Locate every white blood cell.
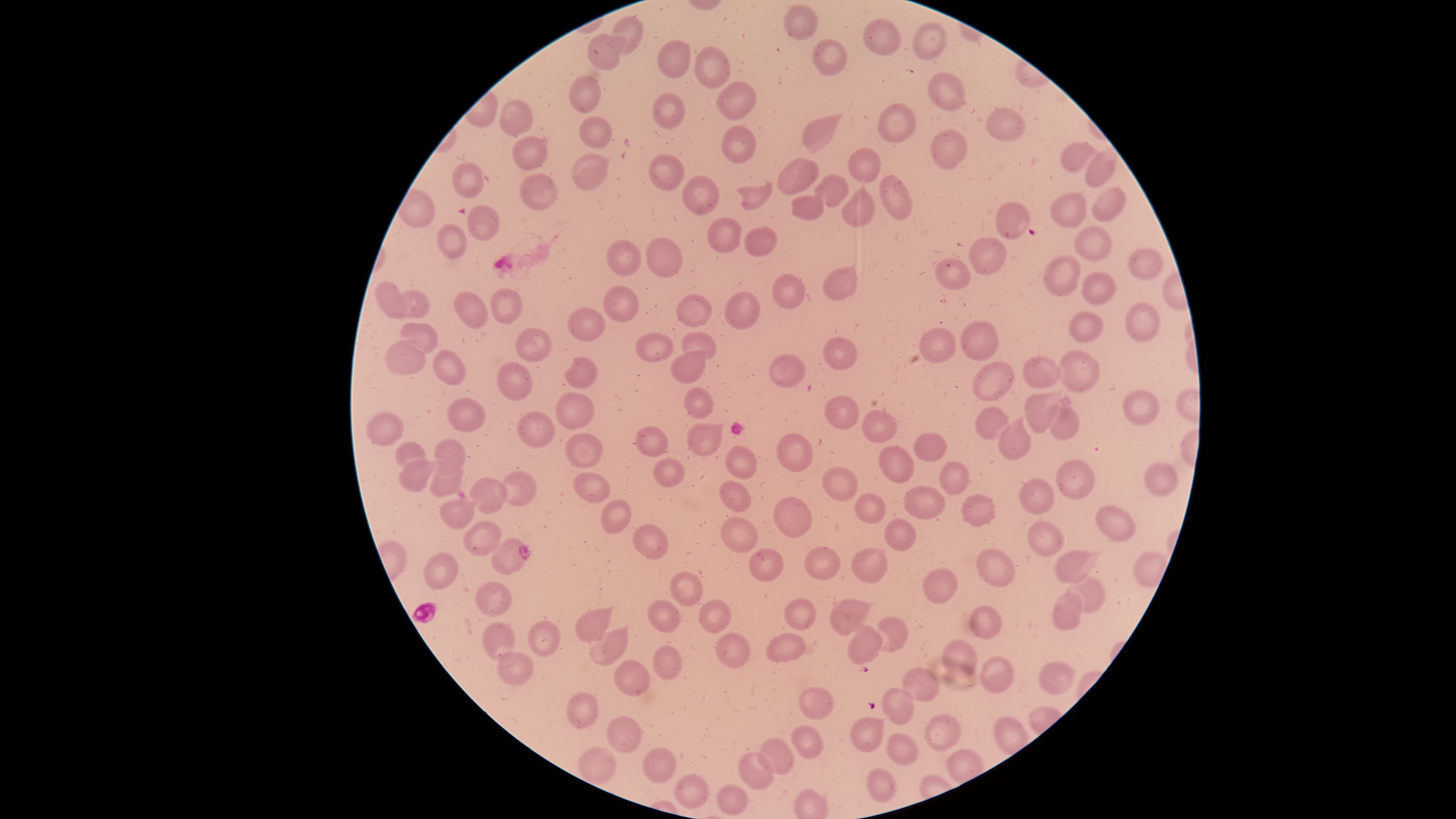
No white blood cells identified.

{
  "stain": "Giemsa",
  "field_of_view": "single",
  "presence": "no malaria parasites identified",
  "uninfected_red_blood_cells": "approximate bounding boxes as [left, top, right, bottom] in pixels: [782, 3, 820, 41], [612, 16, 645, 57], [864, 19, 901, 55], [912, 23, 946, 60], [585, 33, 622, 72], [658, 39, 691, 78], [813, 39, 846, 76], [695, 47, 731, 89], [927, 72, 965, 111], [568, 75, 600, 114], [717, 81, 756, 120], [652, 93, 686, 131], [499, 99, 532, 135], [877, 104, 916, 143], [986, 109, 1026, 143], [802, 115, 840, 153], [579, 116, 611, 148], [721, 126, 755, 164], [931, 129, 966, 169], [512, 136, 547, 170], [1060, 140, 1101, 172], [848, 148, 880, 183], [1084, 151, 1116, 188], [572, 153, 609, 192], [649, 154, 683, 191], [778, 158, 820, 196], [451, 161, 485, 198], [519, 174, 555, 209], [815, 174, 849, 208], [879, 174, 912, 221], [681, 176, 717, 214], [736, 182, 773, 209], [1092, 187, 1124, 222], [841, 188, 875, 226], [1050, 192, 1086, 228], [789, 193, 824, 220], [995, 202, 1030, 240], [466, 205, 499, 240], [706, 217, 742, 254], [436, 223, 467, 258], [1074, 223, 1112, 262], [743, 228, 777, 256], [969, 235, 1005, 274], [645, 237, 682, 278], [605, 240, 641, 276], [1129, 248, 1162, 280], [1044, 256, 1081, 297], [934, 258, 972, 290], [823, 266, 856, 302], [772, 273, 806, 308], [1082, 274, 1116, 306], [374, 281, 409, 318], [602, 286, 637, 321], [490, 288, 521, 325], [394, 290, 429, 319], [725, 291, 761, 329], [454, 293, 489, 329], [676, 295, 710, 325], [1126, 305, 1159, 343], [569, 308, 605, 341], [1069, 311, 1104, 341], [962, 321, 998, 360], [400, 322, 436, 353], [515, 328, 552, 362], [919, 328, 955, 362], [682, 332, 716, 360], [636, 334, 673, 362], [822, 337, 858, 370], [384, 341, 425, 374], [670, 348, 707, 384], [431, 349, 465, 385], [1058, 351, 1099, 391], [769, 354, 806, 388], [1022, 356, 1060, 387], [563, 357, 597, 389], [497, 362, 533, 401], [973, 362, 1014, 402], [683, 388, 714, 419], [1025, 389, 1062, 432], [1124, 389, 1160, 426], [555, 392, 594, 430], [825, 396, 859, 429], [447, 398, 485, 433], [1049, 405, 1081, 440], [975, 407, 1009, 440], [366, 411, 404, 444], [518, 411, 555, 449], [863, 411, 898, 443], [999, 418, 1031, 460], [684, 422, 722, 455], [636, 426, 668, 456], [914, 432, 947, 462], [565, 433, 603, 469], [778, 434, 814, 472], [433, 439, 466, 471], [396, 442, 427, 471], [880, 446, 915, 483], [725, 447, 757, 478], [399, 455, 436, 490], [431, 457, 464, 496], [654, 458, 685, 487], [939, 461, 969, 495], [1056, 461, 1094, 499], [1143, 464, 1177, 495], [823, 466, 858, 501], [500, 471, 537, 507], [571, 472, 611, 503], [470, 477, 507, 513], [1018, 478, 1054, 515], [719, 481, 750, 512], [903, 486, 944, 520], [961, 492, 996, 525], [856, 495, 886, 523], [774, 497, 812, 539], [439, 499, 475, 530], [601, 500, 631, 534], [1096, 506, 1137, 541], [719, 517, 758, 552], [884, 518, 916, 551], [463, 521, 501, 556], [1027, 521, 1063, 557], [633, 524, 668, 559], [491, 540, 526, 575], [805, 547, 840, 579], [851, 548, 887, 583], [978, 548, 1014, 586], [749, 549, 784, 582], [1054, 550, 1095, 584], [424, 552, 457, 591], [924, 569, 956, 604], [669, 571, 702, 606], [1070, 574, 1104, 612], [477, 583, 512, 615], [1052, 590, 1085, 632], [785, 597, 815, 630], [646, 598, 680, 632], [699, 598, 731, 632], [830, 598, 870, 635], [969, 606, 1002, 639], [575, 607, 611, 642], [876, 615, 910, 652], [483, 621, 515, 662], [528, 622, 560, 656], [848, 624, 882, 665], [589, 627, 630, 665], [715, 632, 750, 668], [766, 634, 805, 661], [942, 641, 977, 678], [652, 644, 683, 680], [497, 652, 533, 691], [615, 659, 650, 696], [980, 659, 1015, 692], [1037, 662, 1073, 695], [901, 668, 938, 701], [799, 687, 834, 720], [884, 689, 913, 725], [566, 691, 598, 728], [851, 716, 884, 751], [924, 716, 960, 751], [608, 717, 641, 752], [791, 726, 822, 759], [886, 734, 919, 765], [758, 739, 794, 774], [643, 747, 677, 782], [577, 748, 616, 785], [738, 751, 774, 789], [867, 768, 897, 802], [676, 776, 708, 808], [716, 785, 746, 815]",
  "visible_region": "circular",
  "preparation": "thin smear of blood",
  "capture": "smartphone photograph through the microscope eyepiece",
  "image_size": "1456×819 pixels"
}